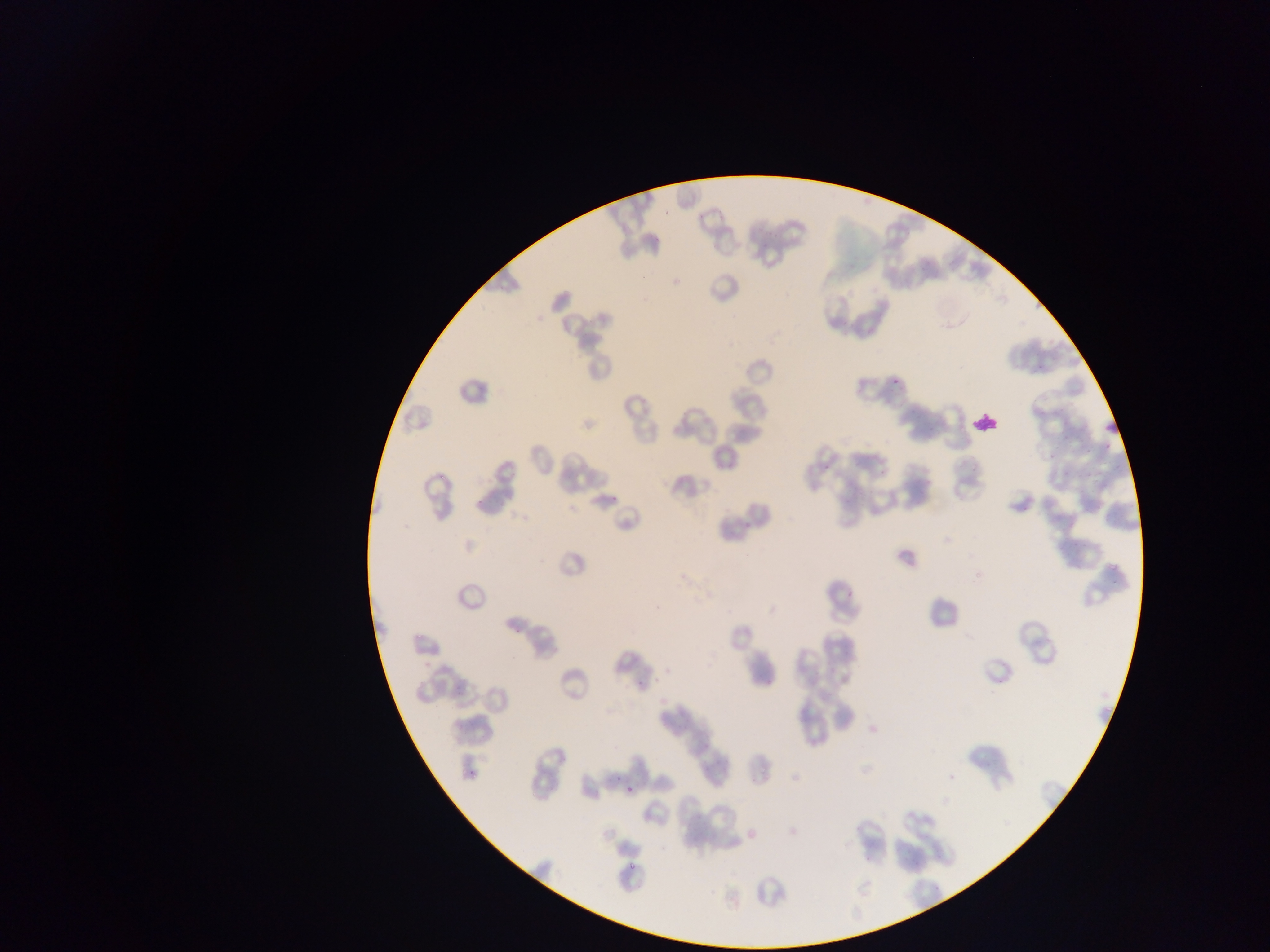
Approximate bounding boxes as left top right bottom in pixels. Leukocyte locations: 971 408 1000 435. Plasmodium parasite locations: 891 379 905 386; 625 784 637 797; 628 863 637 873. One field of view. Thin blood smear. Image is 1270×952 pixels. Sample from Ghana. Photographed through a microscope with a mobile-phone camera.